Outline each blood parasite and name the species.
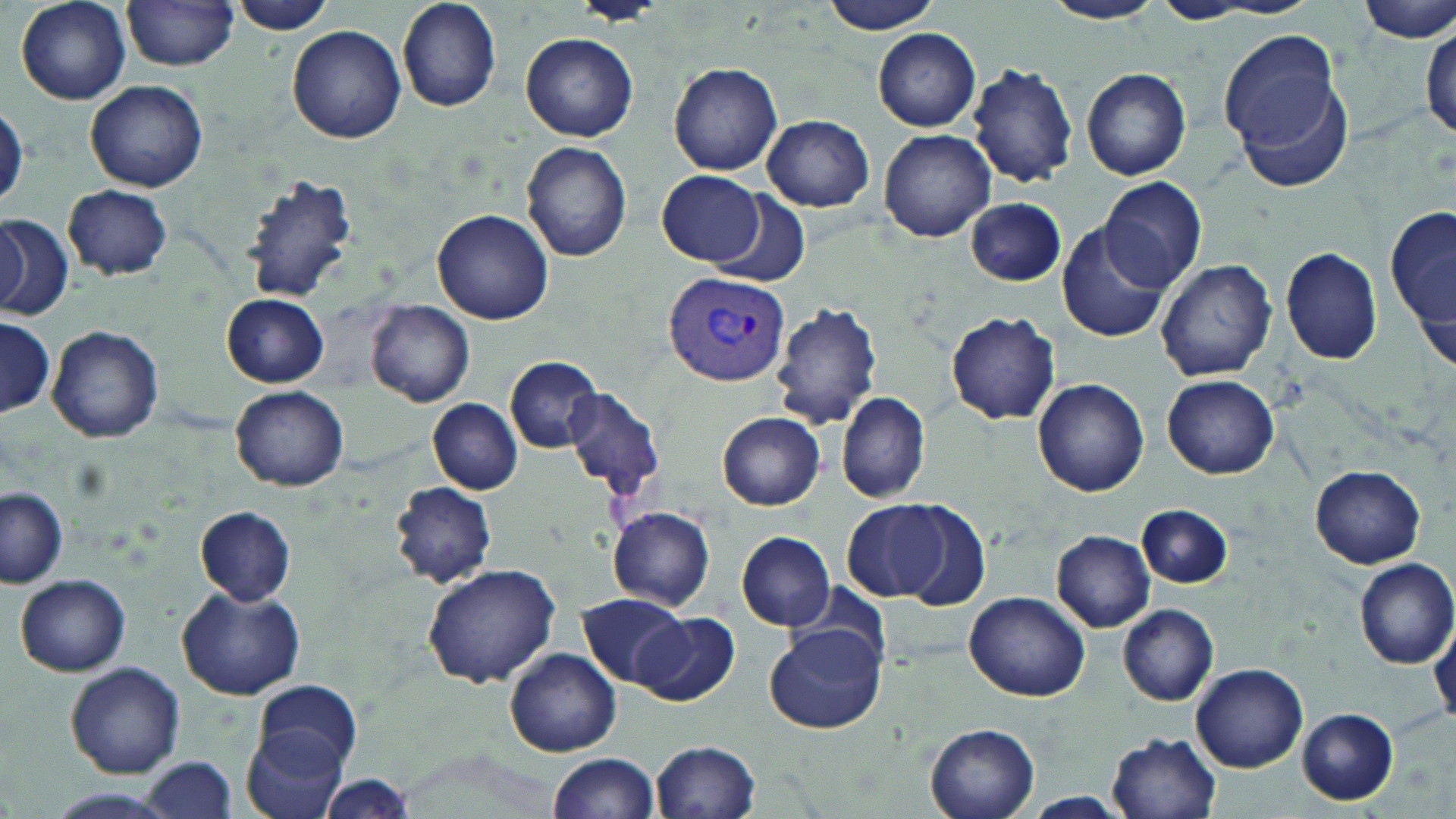
Approximate bounding boxes as (x1,y1)-(x2,y2) corner pairs in pixels.
Plasmodium vivax-infected red blood cells: (663,270)-(789,387).
No Plasmodium falciparum, Plasmodium ovale, Plasmodium malariae, Babesia divergens, or Trypanosoma brucei observed.

slide-level diagnosis = Plasmodium vivax
image size = 1456×819 pixels
preparation = thin blood film
magnification = 1000x
modality = optical microscopy
uninfected red blood cell locations = approximate bounding boxes as (x1,y1)-(x2,y2) corner pairs in pixels: (14,0)-(132,106), (395,0)-(501,111), (571,0)-(666,26), (820,0)-(945,36), (1046,0)-(1162,25), (1355,1)-(1456,45), (122,2)-(241,71), (1149,2)-(1261,24), (231,3)-(340,37), (288,25)-(405,142), (1220,28)-(1347,161), (1421,28)-(1455,148), (874,29)-(982,132), (521,32)-(638,141), (668,62)-(784,175), (967,62)-(1080,186), (1080,67)-(1192,182), (85,80)-(207,192), (913,85)-(1068,215), (1,105)-(26,210), (761,114)-(876,212), (879,128)-(995,242), (520,140)-(632,262), (657,169)-(764,266), (240,174)-(358,304), (1100,176)-(1207,292), (62,184)-(174,279), (706,192)-(809,287), (965,197)-(1065,286), (1388,201)-(1456,358), (433,208)-(553,324), (0,216)-(73,319), (0,219)-(30,314), (1056,220)-(1172,343), (1280,246)-(1383,366), (1155,259)-(1277,381), (222,294)-(328,387), (368,300)-(475,407), (771,302)-(882,430), (947,312)-(1060,426), (0,318)-(56,417), (47,325)-(162,442), (506,356)-(604,452), (1162,375)-(1279,478), (1033,377)-(1149,497), (230,385)-(347,491), (564,385)-(664,501), (837,391)-(931,504), (428,399)-(524,496), (718,411)-(827,510), (1311,466)-(1426,568), (388,480)-(498,589), (0,489)-(68,587), (843,501)-(951,604), (900,502)-(990,609), (1137,505)-(1233,589), (606,506)-(717,612), (195,507)-(296,606), (1053,530)-(1155,630), (737,532)-(835,630), (1355,558)-(1456,667), (421,563)-(560,688), (15,574)-(131,675), (177,586)-(305,701), (964,590)-(1092,701), (578,593)-(688,688), (1118,604)-(1219,705), (636,612)-(739,705), (766,623)-(886,735), (1430,623)-(1456,729), (506,648)-(620,756), (1191,662)-(1307,772), (66,663)-(185,778), (255,681)-(363,772), (1298,709)-(1396,804), (927,725)-(1040,819), (242,726)-(349,819), (1108,732)-(1223,818), (650,740)-(762,819), (547,752)-(661,819), (143,758)-(237,815), (320,775)-(415,818), (1023,793)-(1128,817)
field of view = single
stain = May-Grünwald-Giemsa